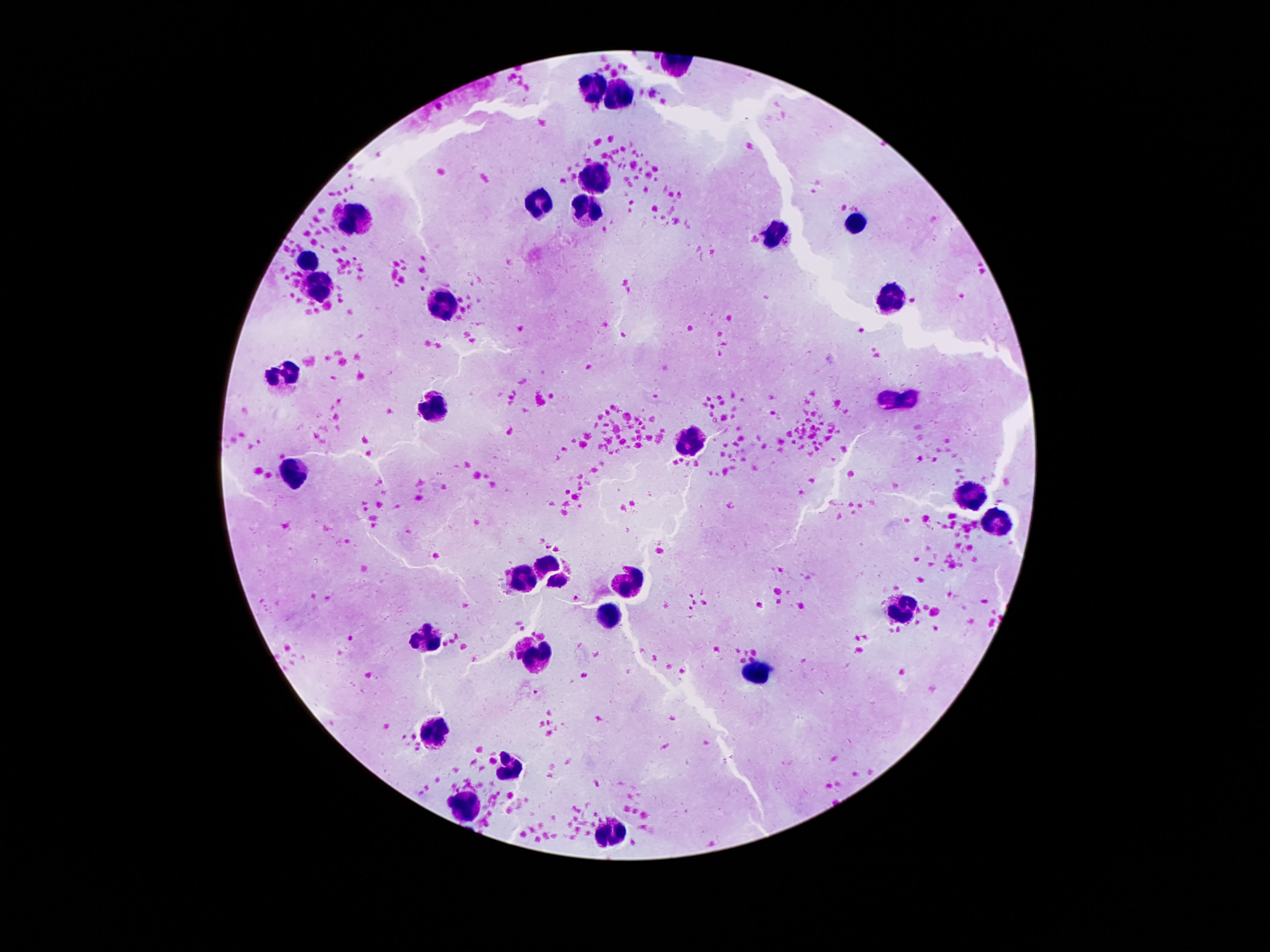

field_of_view: single
stain: Giemsa
patient_malaria_status: not infected
leukocyte_locations: 'approximate object centers, in pixels from the top-left corner: (x=590, y=85), (x=619, y=94), (x=594, y=177), (x=539, y=206), (x=584, y=214), (x=354, y=217), (x=858, y=224), (x=776, y=236), (x=307, y=259), (x=320, y=283), (x=893, y=296), (x=440, y=303), (x=283, y=374), (x=897, y=402), (x=436, y=409), (x=690, y=443), (x=293, y=476), (x=977, y=501), (x=995, y=522), (x=551, y=573), (x=524, y=575), (x=631, y=579), (x=907, y=609), (x=608, y=618), (x=430, y=640), (x=535, y=654), (x=760, y=672), (x=434, y=728), (x=506, y=761), (x=465, y=801), (x=610, y=831)'
capture: smartphone camera through the microscope eyepiece
magnification: 100x
preparation: thick blood smear
image_size: 1270×952 pixels